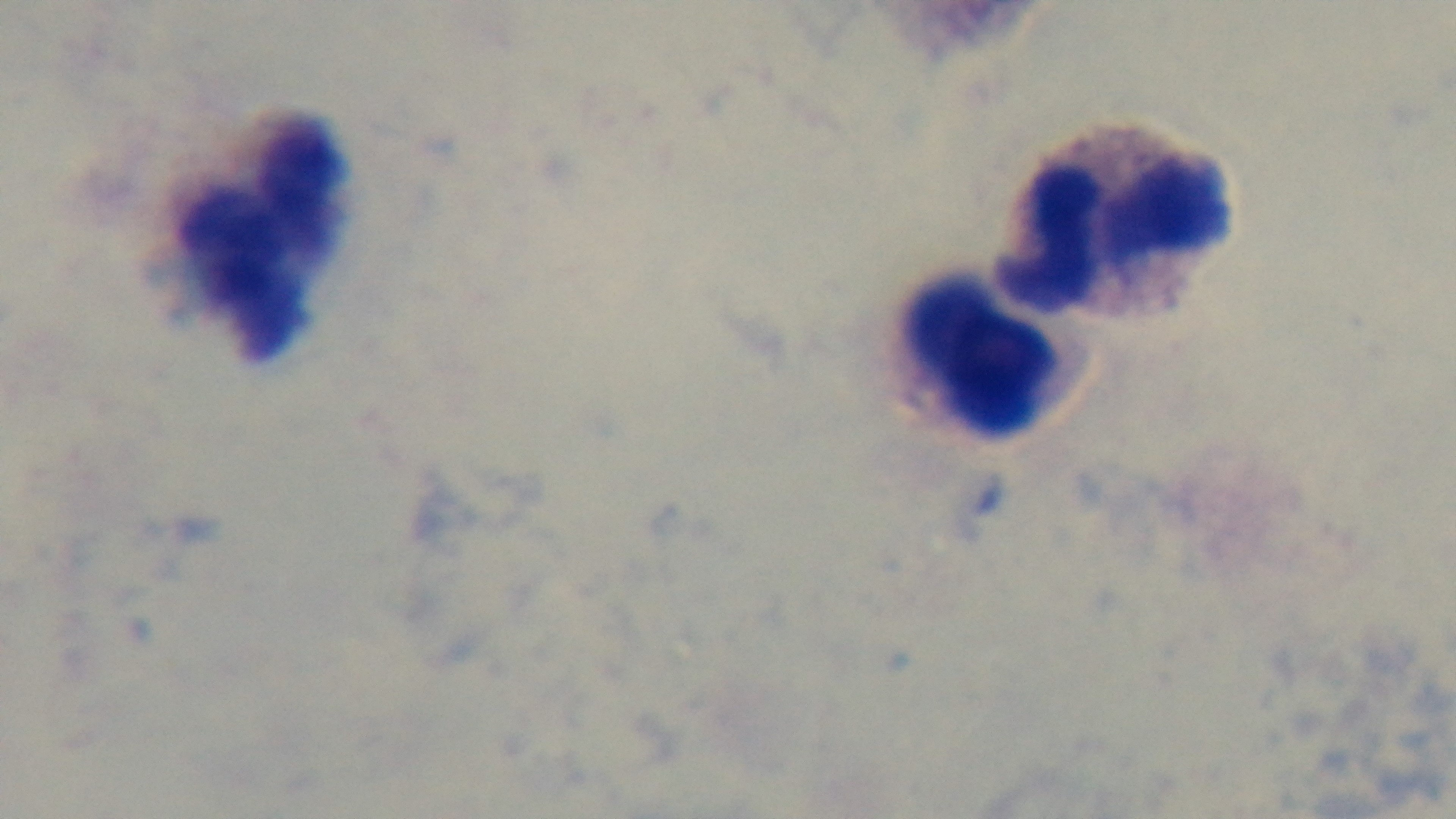

Summary:
  - Malaria status: negative
  - Stain: Giemsa
  - Modality: light microscopy
  - Objective: 100x oil immersion
  - Capture: mounted 4K digital camera
  - Field of view: one from the slide
  - Preparation: thick blood film